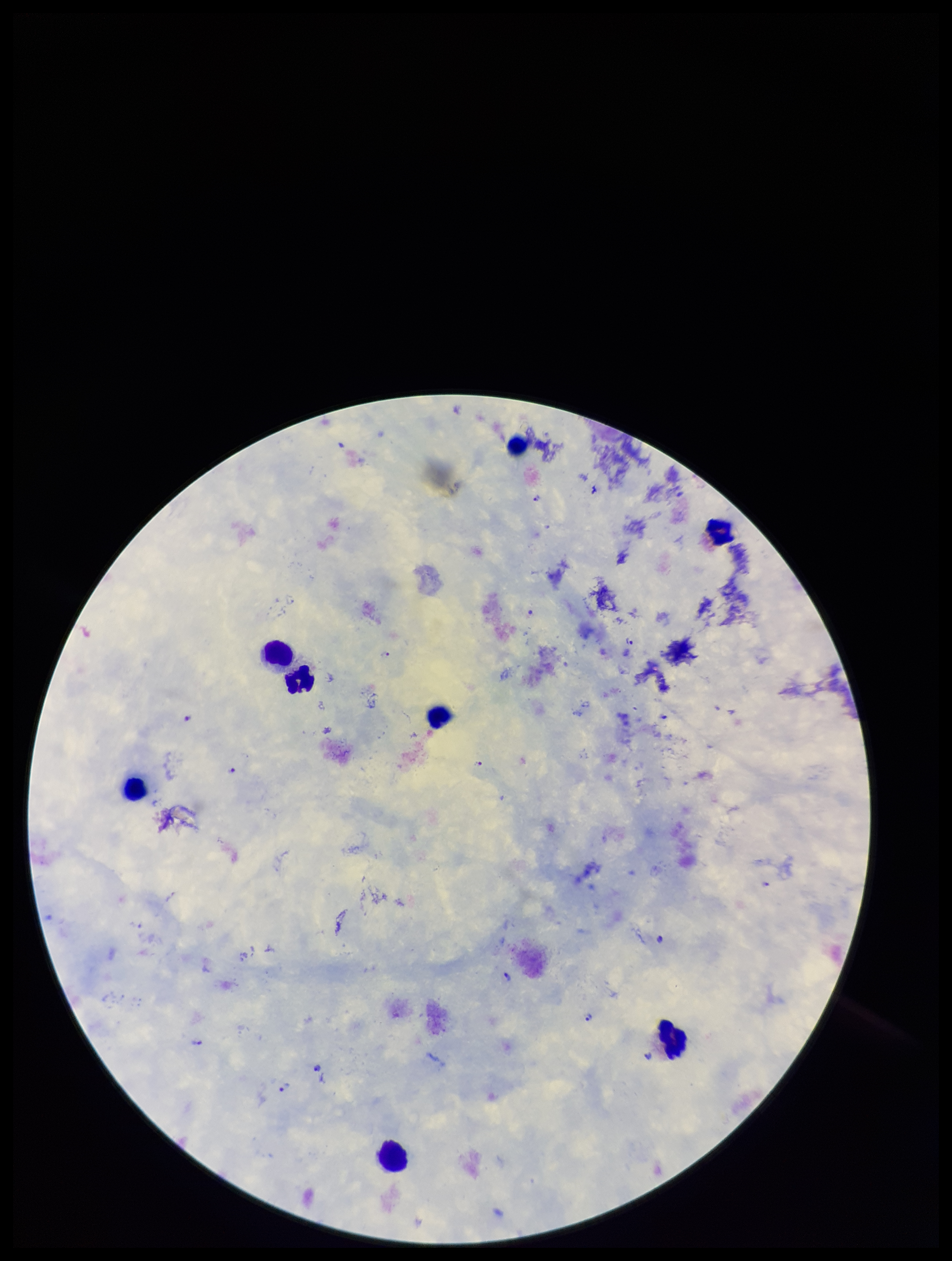

Summary:
  - Capture: smartphone photograph through the microscope eyepiece
  - Parasite count: 15
  - Stain: Giemsa
  - Field of view: single
  - Preparation: thick smear
  - Patient malaria status: infected
  - Leukocyte count: 8
  - Plasmodium parasites: identified
  - Species reported for this patient: Plasmodium falciparum
  - Image size: 952×1261 pixels